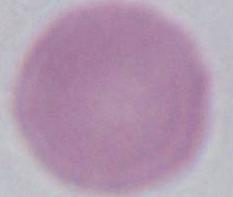
Summary:
  - Magnification: 1000x
  - Modality: micrograph
  - Identification: red blood cell